Evaluate for Plasmodium parasites.
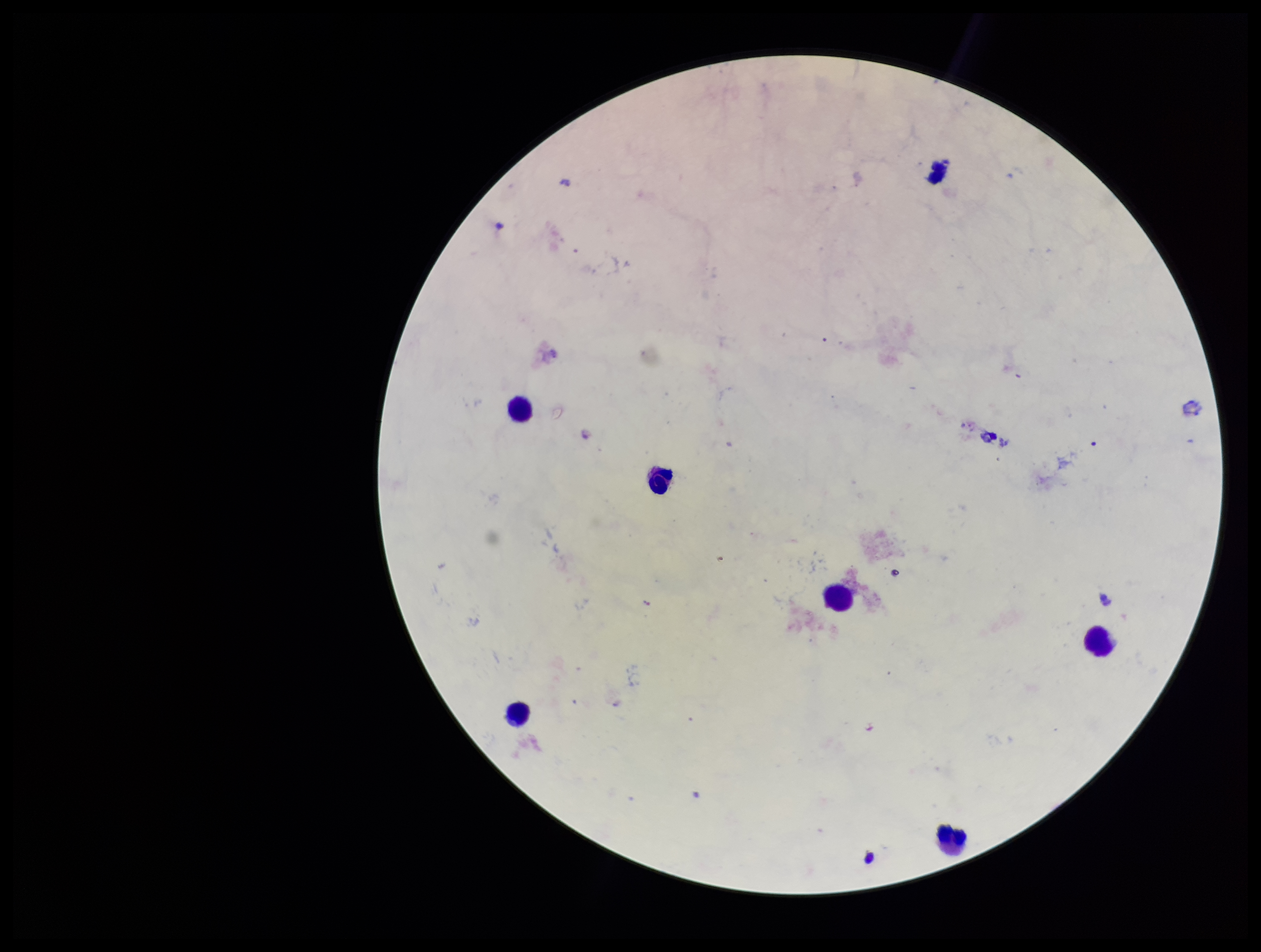
None identified.

Summary:
  - Image size: 1261×952 pixels
  - Capture: smartphone photograph through the microscope eyepiece
  - Preparation: thick blood smear
  - Parasite count: 0
  - Stain: Giemsa
  - Field of view: one from this slide
  - Leukocyte count: 6
  - Patient malaria status: negative